Look for Plasmodium parasites.
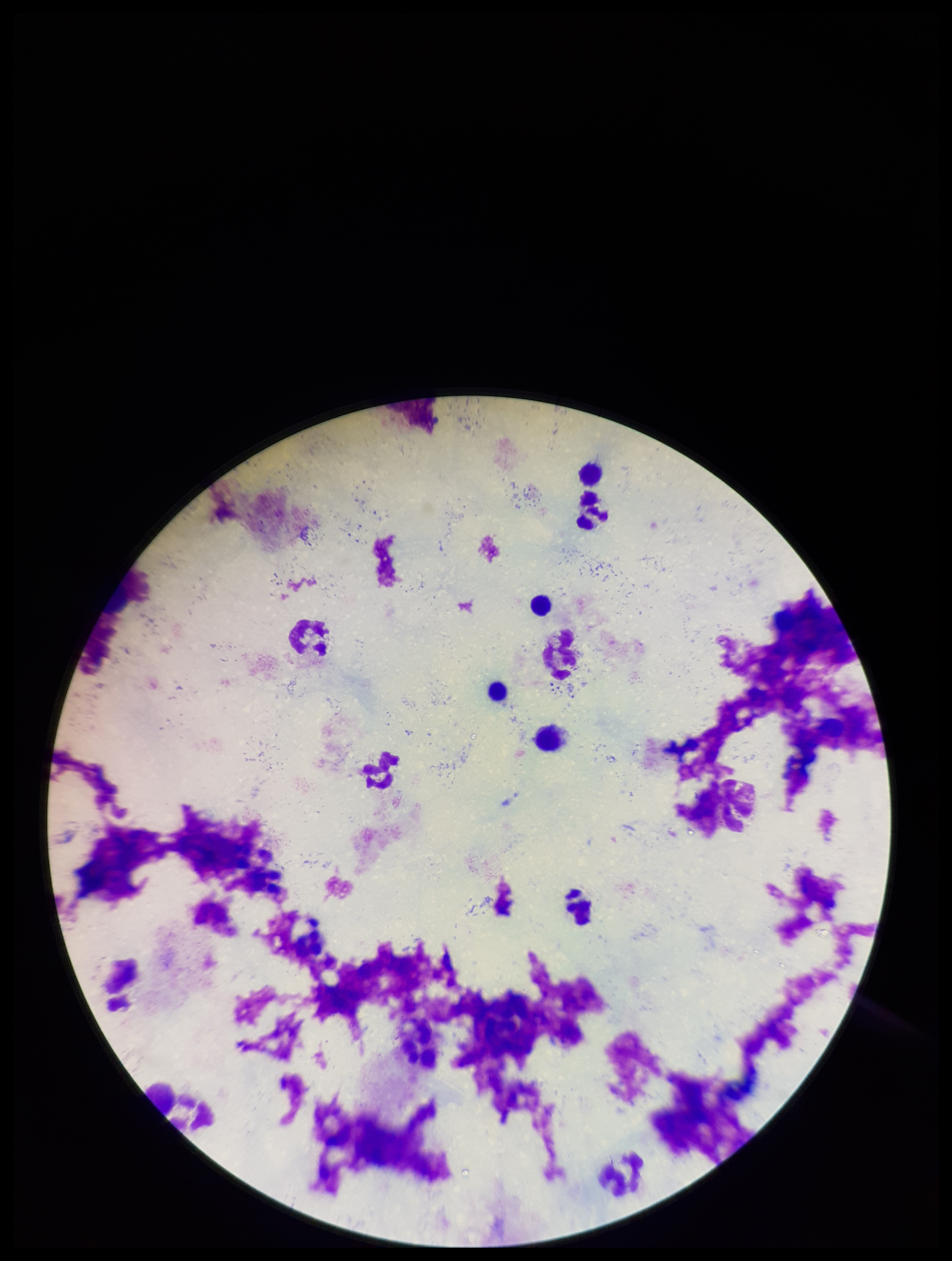
None detected.

Summary:
  - Leukocyte count: 4
  - Preparation: thick
  - Patient malaria status: negative
  - Field of view: one from this slide
  - Image size: 952×1261 pixels
  - Stain: Giemsa
  - Capture: smartphone photograph through the microscope eyepiece
  - Parasite count: 0